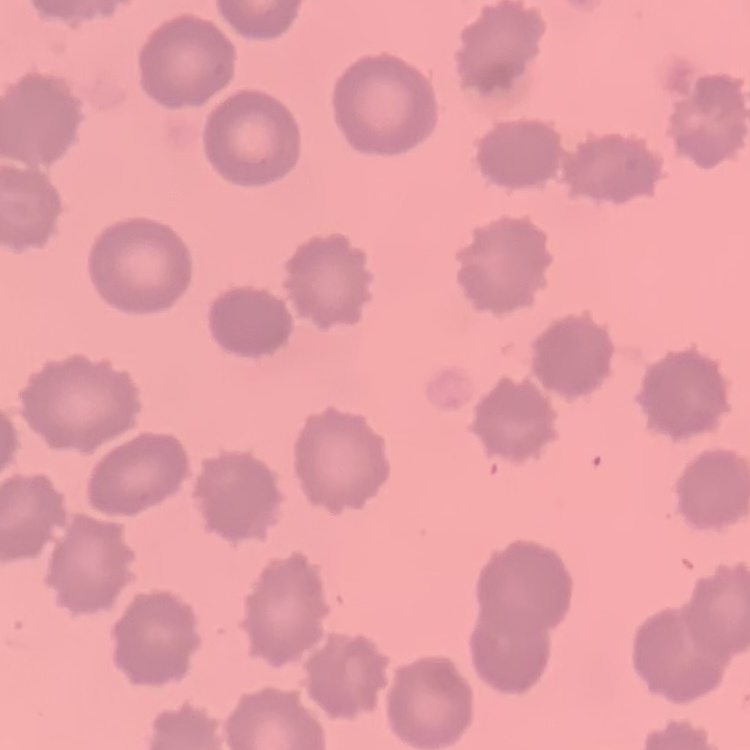

Summary:
  - Erythrocyte morphology: no rouleaux formation
  - Stain: Field's or Giemsa
  - Preparation: thin peripheral smear
  - Image type: square crop of a larger photomicrograph